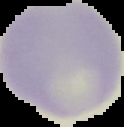
Image is 124×127 pixels. Result: negative for Plasmodium parasites. From a thin blood film. The area outside the segmented cell region is set to black.